Identify the cell.
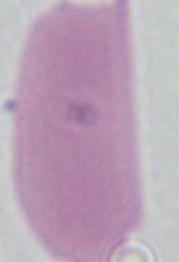

This is an erythrocyte.

Micrograph. Captured at 1000x magnification.